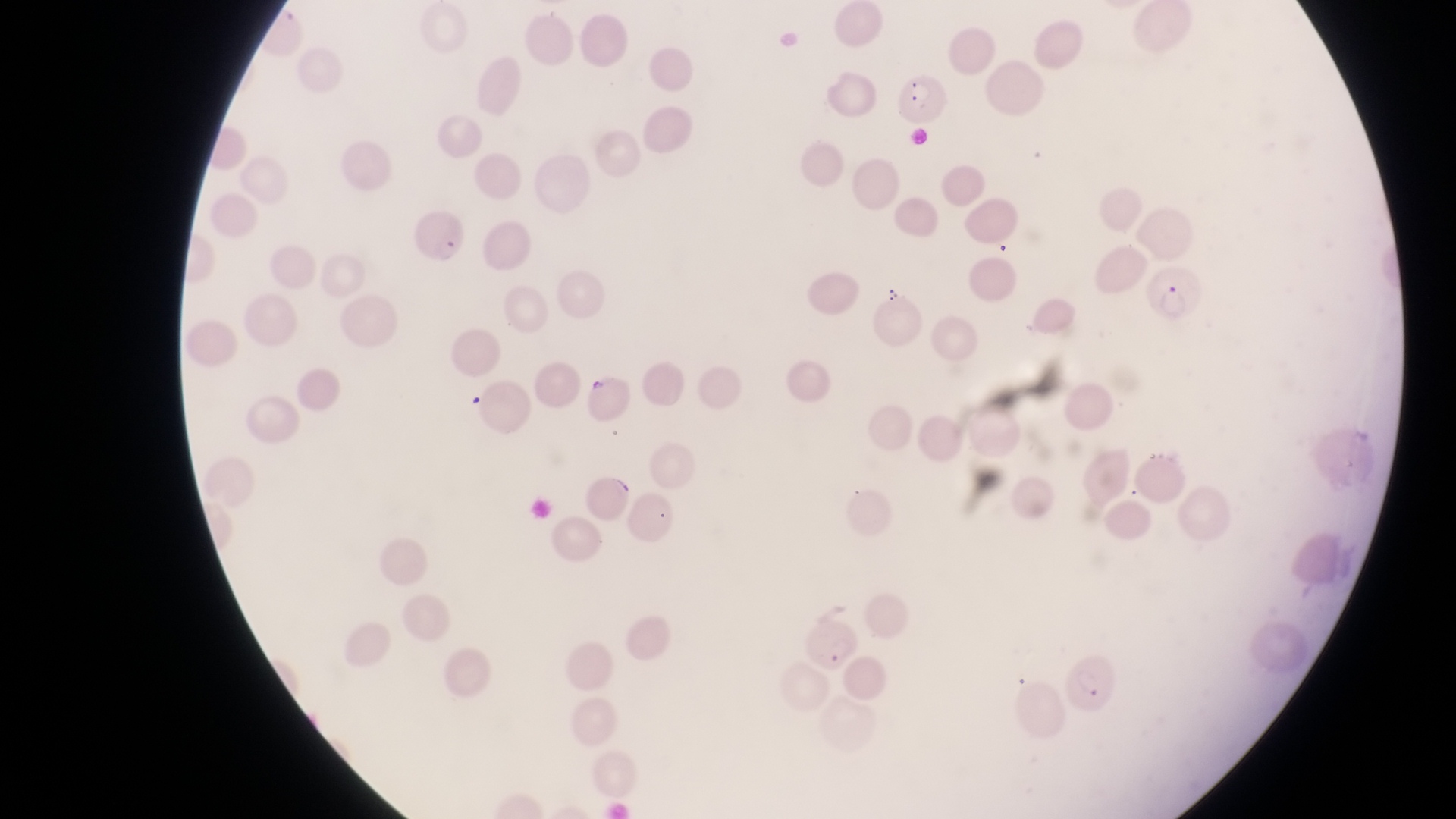
image size = 1456×819 pixels
capture = smartphone photograph through the eyepiece of an Olympus CX-23 microscope
artifact (platelet-like body, stain precipitate, or debris) locations = approximate bounding boxes as (left, top, right, bottom) in pixels: (880, 287, 906, 306)
country = Uganda
preparation = thin blood film
field of view = single
magnification = 1000x
parasitised red blood cell locations = approximate bounding boxes as (left, top, right, bottom) in pixels: (898, 74, 951, 127), (416, 212, 471, 271), (1149, 265, 1202, 326), (1063, 642, 1118, 715)